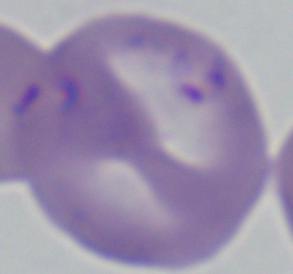
Summary:
  - Modality: micrograph
  - Magnification: 1000x
  - Identification: Babesia